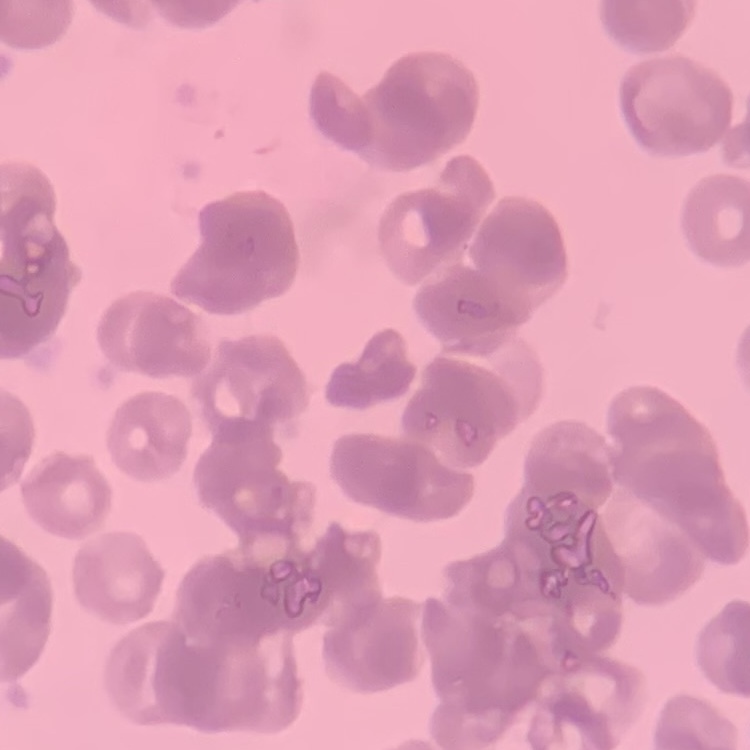 The red blood cells show rouleaux formation. Thin blood film. One tile cut from a larger photomicrograph. Stained with either Field's or Giemsa.